Classify this cell by malaria status.
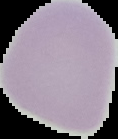
It is uninfected.

preparation = thin blood smear
image size = 118×139 pixels
image type = segmented cell region with the area outside set to black